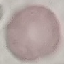
malaria status = uninfected
preparation = thin blood smear
image type = cell patch, automatically extracted from a larger field of view and resized to 64 × 64 pixels
capture = smartphone through the microscope eyepiece
stain = Giemsa